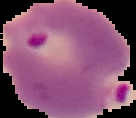

Image is 136×118 pixels. From a thin blood smear. Malaria status: parasitized. The area outside the segmented cell region is set to black.